Assess this cell for malaria.
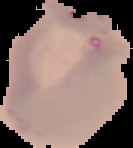
Uninfected.

image_type: cell region segmented out of the field of view; surrounding area masked to black
preparation: thin blood film
image_size: 133×148 pixels